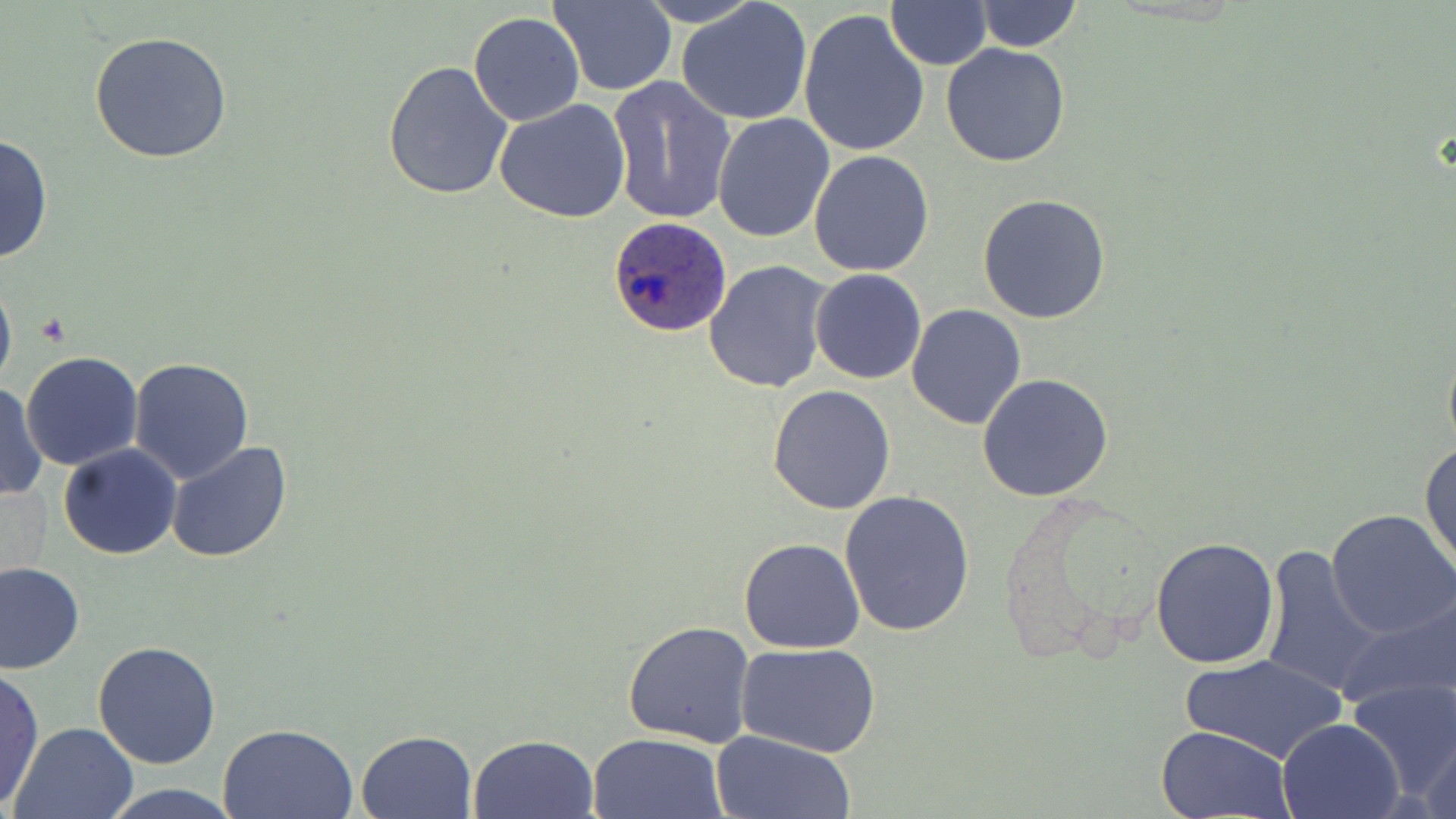

Summary:
  - Coordinate format: approximate bounding boxes as (x1,y1)-(x2,y2) corner pairs in pixels
  - Uninfected red blood cell locations: (547,0)-(677,96), (634,0)-(765,27), (678,0)-(813,126), (974,0)-(1083,53), (886,3)-(993,68), (799,10)-(931,161), (468,11)-(585,126), (88,30)-(233,163), (940,43)-(1071,167), (383,59)-(513,200), (607,75)-(736,227), (493,98)-(632,224), (712,114)-(835,243), (1,133)-(55,266), (808,150)-(935,278), (977,193)-(1110,325), (703,260)-(835,395), (0,265)-(17,402), (810,268)-(926,385), (906,303)-(1029,429), (1441,330)-(1456,465), (21,351)-(143,471), (128,357)-(255,483), (977,372)-(1115,502), (0,382)-(48,503), (767,385)-(896,515), (1419,438)-(1455,577), (165,442)-(294,565), (58,444)-(182,560), (839,489)-(974,637), (1327,510)-(1456,642), (1150,536)-(1279,669), (738,537)-(867,654), (1259,545)-(1382,698), (0,562)-(84,674), (1334,591)-(1456,715), (623,621)-(755,748), (93,641)-(222,769), (736,641)-(883,758), (1182,653)-(1345,764), (0,667)-(46,809), (1348,678)-(1456,806), (1278,717)-(1404,818), (8,721)-(139,818), (217,722)-(359,819), (1156,724)-(1295,818), (1419,727)-(1456,819), (357,729)-(477,817), (710,730)-(855,818), (587,731)-(728,819), (467,733)-(598,818), (99,782)-(242,819)
  - Plasmodium ovale-infected red blood cell locations: (606,216)-(731,337)
  - Slide-level diagnosis: Plasmodium ovale
  - Modality: optical microscopy
  - Image size: 1456×819 pixels
  - Field of view: one of a larger specimen
  - Stain: May-Grünwald-Giemsa
  - Magnification: 1000x
  - Preparation: thin blood film